Identify the parasite.
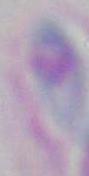

Toxoplasma gondii.

magnification = 1000x
modality = micrograph